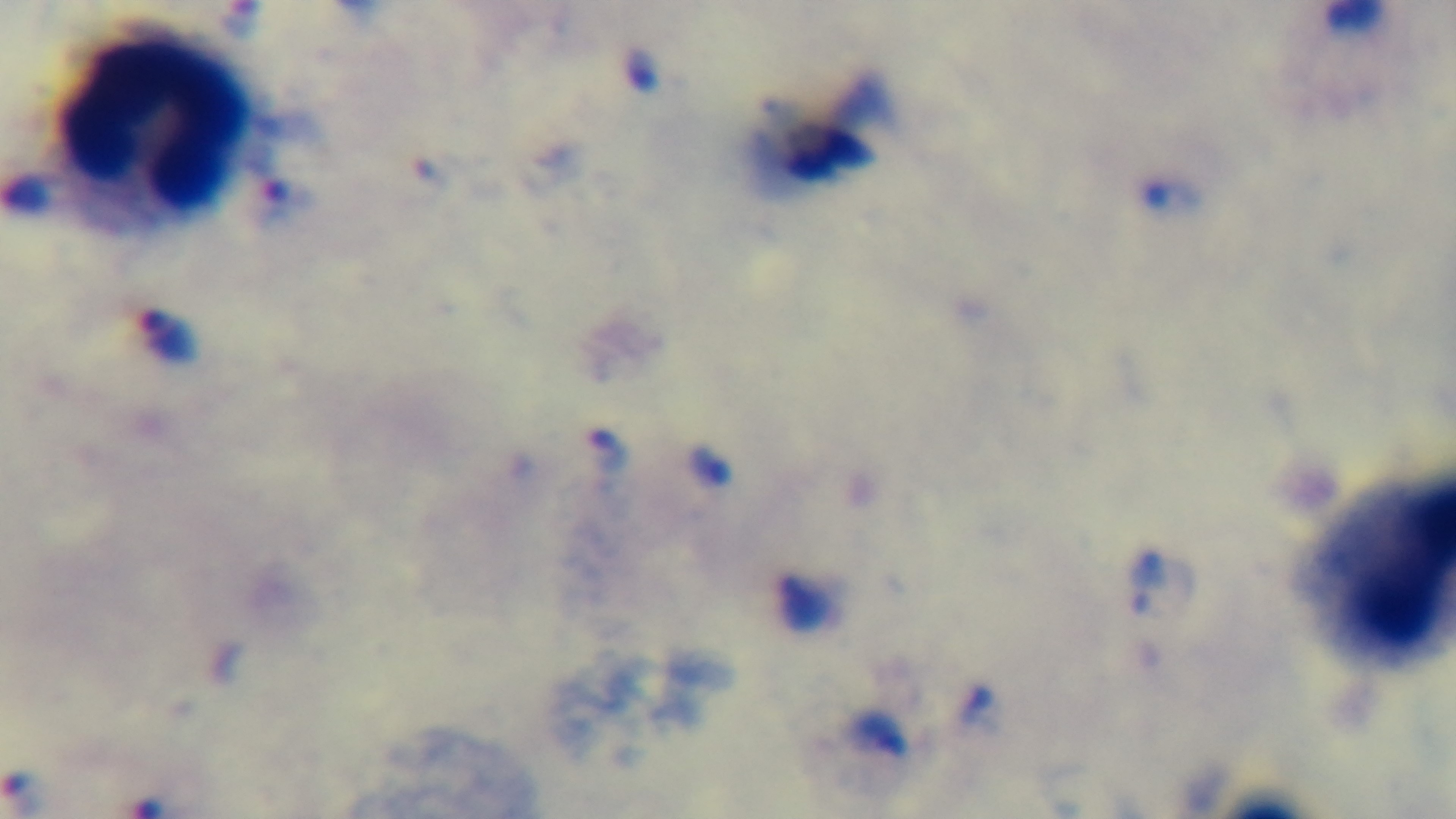
One field from the slide. Giemsa-stained. Preparation: thick blood film. Oil-immersion objective, 100x. Photomicrograph. Captured with a mounted 4K digital camera. Malaria status: infected.